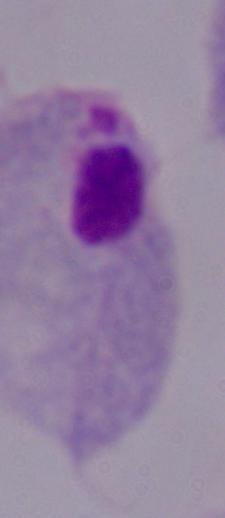
Summary:
  - Modality: photomicrograph
  - Identification: trichomonad
  - Magnification: 1000x